Classify this cell by malaria status.
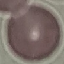
It is uninfected.

Summary:
  - Capture: smartphone camera at the microscope eyepiece
  - Stain: Giemsa
  - Image type: cell patch, automatically extracted from a larger field of view and resized to 64 × 64 pixels
  - Preparation: thin blood film